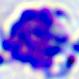
A leukocyte is shown. Micrograph. 400x magnification.